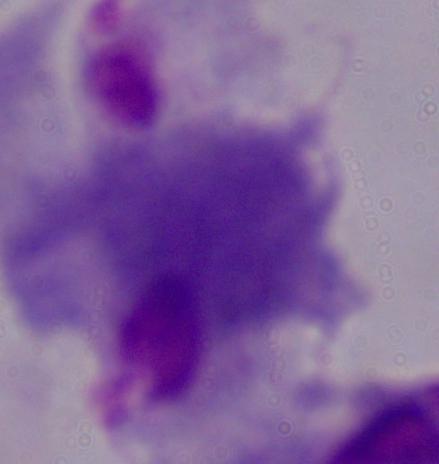
{
  "modality": "micrograph",
  "identification": "trichomonad",
  "magnification": "1000x"
}